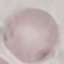
Malaria status: uninfected. Thin blood film. Giemsa stain. Automatically extracted cell patch, resized to 64 × 64 pixels. Acquired by smartphone through the microscope eyepiece.